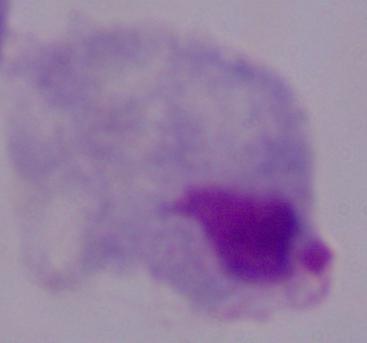

Summary:
  - Identification: trichomonad
  - Magnification: 1000x
  - Modality: photomicrograph